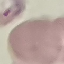

{
  "result": "malaria parasites identified",
  "preparation": "thin blood film",
  "capture": "smartphone through the microscope eyepiece",
  "image_type": "cell patch, automatically extracted from a larger field of view and resized to 64 × 64 pixels",
  "stain": "Giemsa"
}